Assess this cell for malaria.
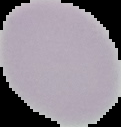
It is uninfected.

Cell region segmented out of the field of view; the surrounding area is masked to black. Image is 121×127 pixels. From a thin blood film.